Name the blood parasite species.
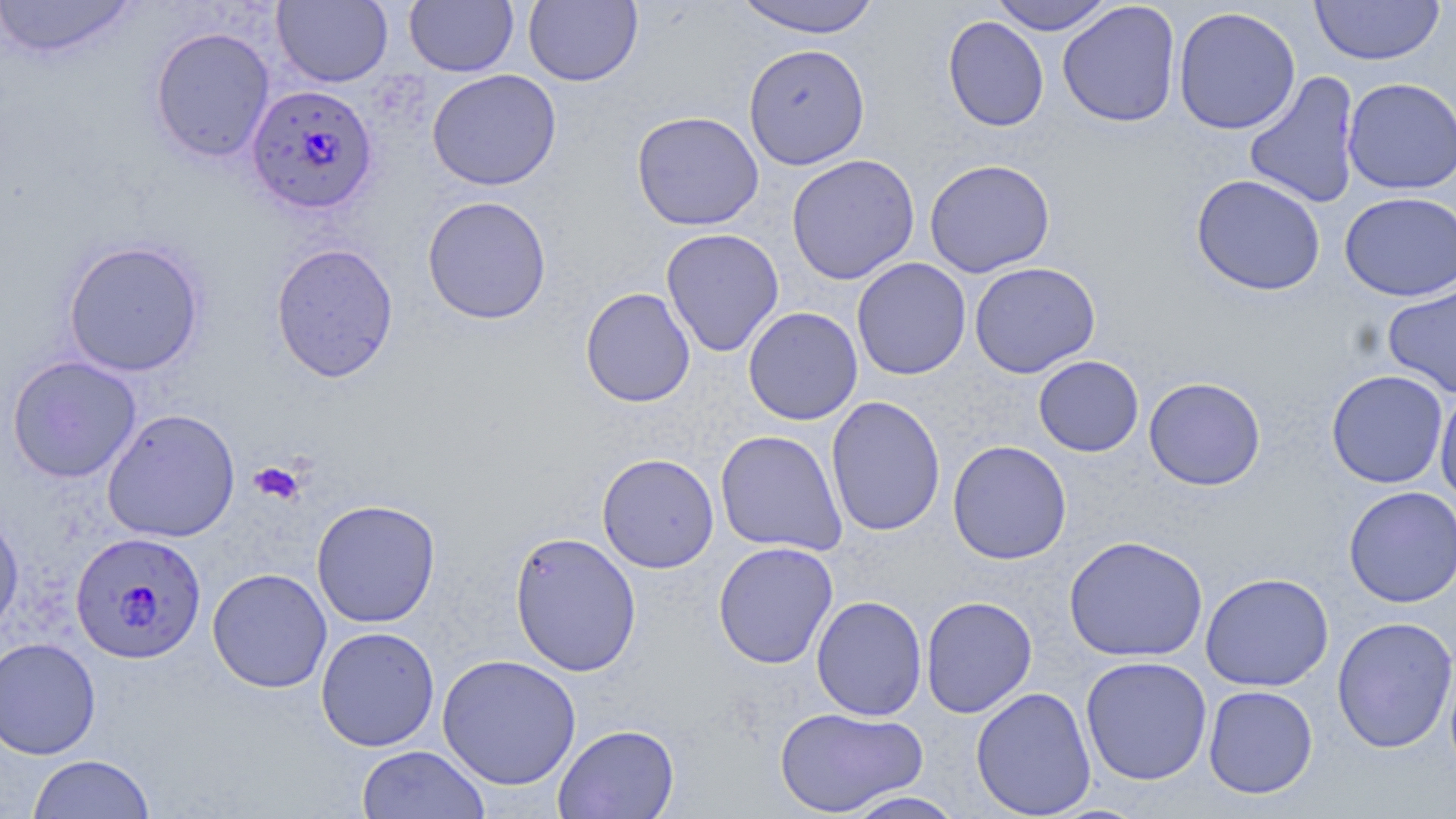

Plasmodium falciparum.

Summary:
  - Coordinate format: approximate bounding boxes as (x1, y1, x2, y2) in pixels
  - Uninfected red blood cell locations: (0, 0, 137, 60), (272, 0, 393, 87), (404, 0, 518, 76), (523, 0, 642, 87), (732, 0, 882, 38), (989, 0, 1115, 35), (1310, 0, 1445, 66), (1058, 2, 1181, 127), (1173, 6, 1301, 135), (943, 16, 1048, 132), (149, 26, 275, 163), (743, 43, 870, 170), (427, 68, 561, 191), (1243, 71, 1361, 209), (1342, 77, 1456, 195), (649, 110, 770, 356), (631, 111, 764, 231), (786, 153, 920, 285), (923, 158, 1055, 278), (1191, 174, 1326, 296), (1339, 191, 1456, 301), (422, 195, 552, 324), (661, 227, 784, 357), (62, 240, 206, 377), (270, 242, 399, 382), (851, 257, 971, 380), (969, 261, 1101, 378), (1382, 281, 1456, 399), (580, 287, 696, 407), (742, 306, 863, 425), (7, 355, 142, 483), (1033, 355, 1144, 456), (1326, 370, 1449, 488), (1144, 376, 1266, 491), (1434, 386, 1456, 505), (826, 395, 946, 537), (101, 408, 240, 543), (715, 430, 847, 555), (947, 440, 1071, 564), (597, 452, 719, 573), (1343, 485, 1456, 607), (311, 499, 441, 628), (0, 508, 24, 640), (509, 530, 642, 676), (1063, 535, 1208, 662), (713, 541, 838, 670), (207, 568, 332, 693), (1200, 572, 1334, 692), (811, 595, 927, 721), (920, 596, 1037, 718), (1332, 616, 1456, 753), (315, 626, 440, 751), (0, 637, 101, 760), (436, 654, 581, 790), (1080, 655, 1213, 785), (1203, 685, 1318, 799), (971, 686, 1096, 818), (774, 706, 927, 817), (553, 723, 680, 819), (356, 745, 490, 819), (27, 754, 155, 818), (842, 790, 967, 818)
  - Plasmodium falciparum-infected red blood cell locations: (244, 84, 379, 216), (71, 531, 207, 664)
  - Platelet locations: (249, 461, 305, 505)
  - Modality: optical microscopy
  - Preparation: thin blood film
  - Stain: May-Grünwald-Giemsa
  - Image size: 1456×819 pixels
  - Magnification: 1000x
  - Field of view: single